Describe the morphology of the erythrocytes.
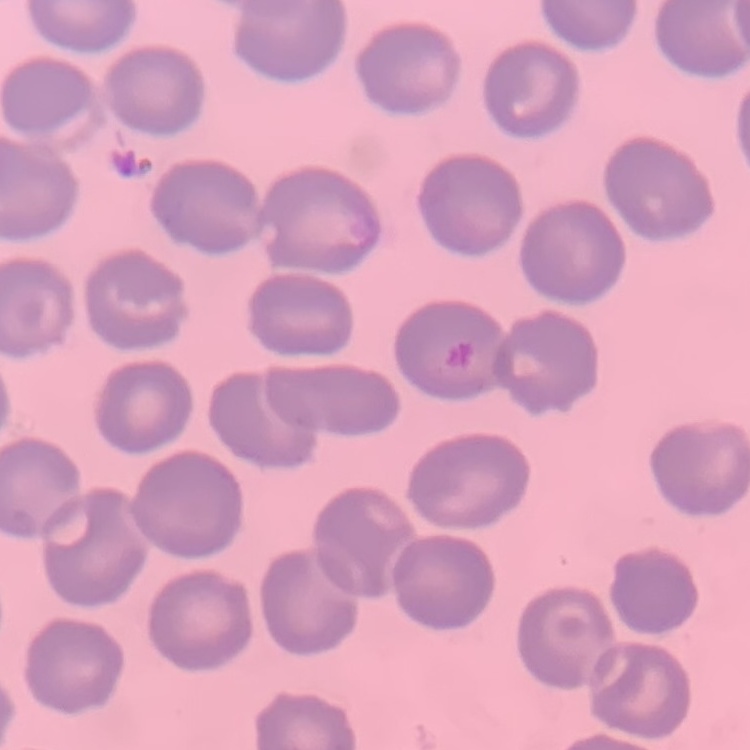
No rouleaux formation.

Square crop of a larger photomicrograph. Stained with either Field's or Giemsa. Thin peripheral smear.